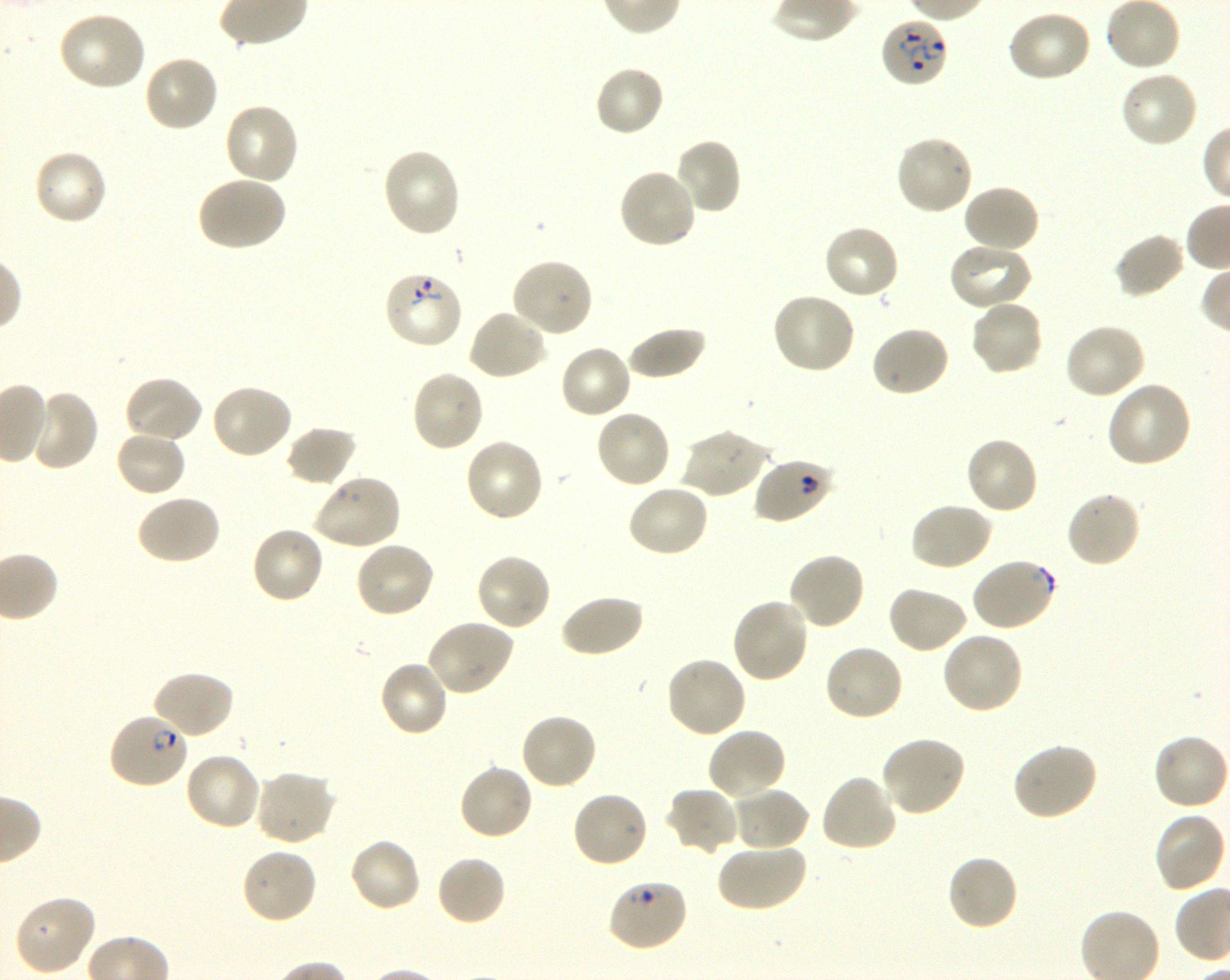

Not every red blood cell is marked. A life-cycle stage — or a range of stages, where the recorded stages span more than one — follows each staged infected red blood cell.
locations of red blood cells of indeterminate infection status = approximate bounding boxes as (x1, y1, x2, y2) in pixels: (754, 456, 835, 525), (970, 557, 1057, 632), (607, 879, 690, 952)
preparation = thin blood film
culture = in-vitro P. falciparum strain 3D7, shaking
field of view = one from this slide
objective = 100x, oil immersion, numerical aperture 1.30
donor blood group = O+
stain = Giemsa
locations of uninfected red blood cells = approximate bounding boxes as (x1, y1, x2, y2) in pixels: (1007, 8, 1093, 82), (56, 11, 148, 93), (143, 54, 219, 133), (594, 65, 666, 139), (1119, 71, 1200, 149), (223, 101, 299, 186), (894, 134, 975, 216), (673, 138, 742, 216), (381, 147, 463, 239), (32, 149, 109, 227), (618, 167, 698, 250), (195, 175, 287, 253), (962, 184, 1041, 254), (821, 223, 900, 300), (1113, 232, 1187, 300), (948, 242, 1034, 312), (510, 258, 594, 338), (771, 292, 857, 376), (969, 298, 1044, 376), (467, 308, 549, 382), (1064, 322, 1146, 400), (869, 324, 950, 398), (625, 325, 706, 381), (558, 344, 632, 421), (409, 368, 485, 454), (122, 375, 203, 445), (1106, 381, 1194, 469), (208, 384, 294, 461), (25, 389, 99, 473), (594, 408, 671, 490), (285, 425, 358, 487), (680, 427, 768, 499), (114, 429, 188, 498), (965, 435, 1040, 515), (464, 437, 545, 523), (311, 474, 402, 551), (626, 483, 710, 559), (1064, 490, 1142, 570), (135, 494, 222, 566), (909, 501, 993, 572), (250, 524, 326, 605), (354, 541, 436, 620), (475, 552, 552, 632), (787, 552, 867, 631), (887, 584, 969, 654), (558, 593, 644, 659), (730, 596, 810, 684), (425, 619, 515, 697), (941, 630, 1025, 715), (823, 642, 906, 722), (664, 655, 748, 739), (377, 660, 450, 739), (150, 669, 235, 741), (519, 711, 598, 790), (707, 727, 788, 802), (1152, 733, 1230, 811), (880, 736, 968, 818), (1011, 741, 1099, 822), (184, 751, 262, 831), (458, 762, 534, 842), (253, 769, 337, 847), (819, 773, 899, 853), (729, 786, 810, 851), (666, 787, 741, 858), (570, 789, 651, 867), (1153, 811, 1228, 893), (348, 837, 422, 913), (716, 841, 807, 913), (240, 847, 317, 925), (945, 853, 1020, 932), (435, 854, 507, 927), (13, 893, 96, 976)
image size = 1230×980 pixels
locations of infected red blood cells = approximate bounding boxes as (x1, y1, x2, y2) in pixels: (879, 16, 948, 89) ring; (383, 268, 464, 350) ring; (108, 711, 190, 789) ring